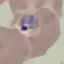

{
  "malaria_status": "parasitized",
  "capture": "smartphone through the microscope eyepiece",
  "stain": "Giemsa",
  "preparation": "thin blood film",
  "image_type": "cell patch, automatically extracted from a larger field of view and resized to 64 × 64 pixels"
}